Comment on the morphology of the erythrocytes.
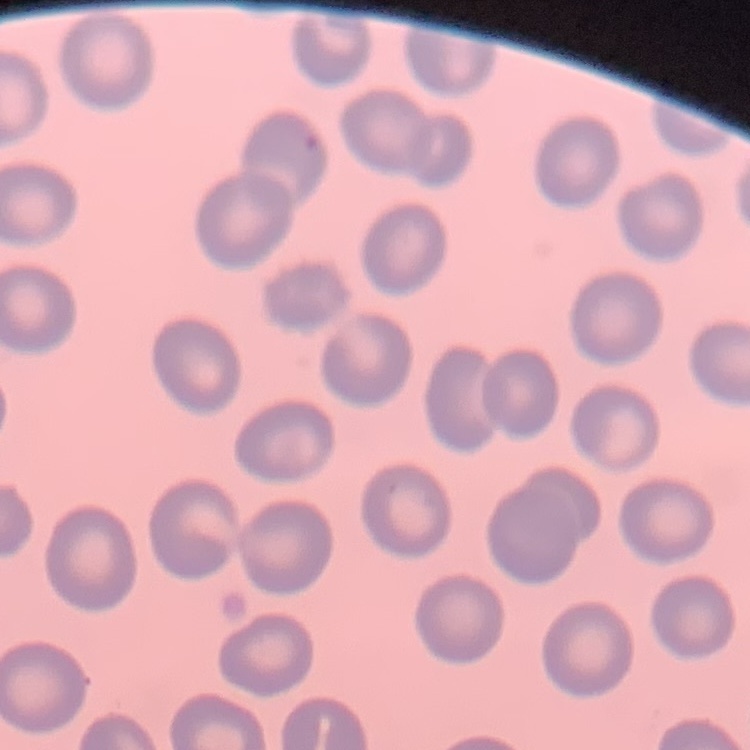

They show no rouleaux formation.

Field's or Giemsa stain. Square crop of a larger photomicrograph. Thin peripheral smear.